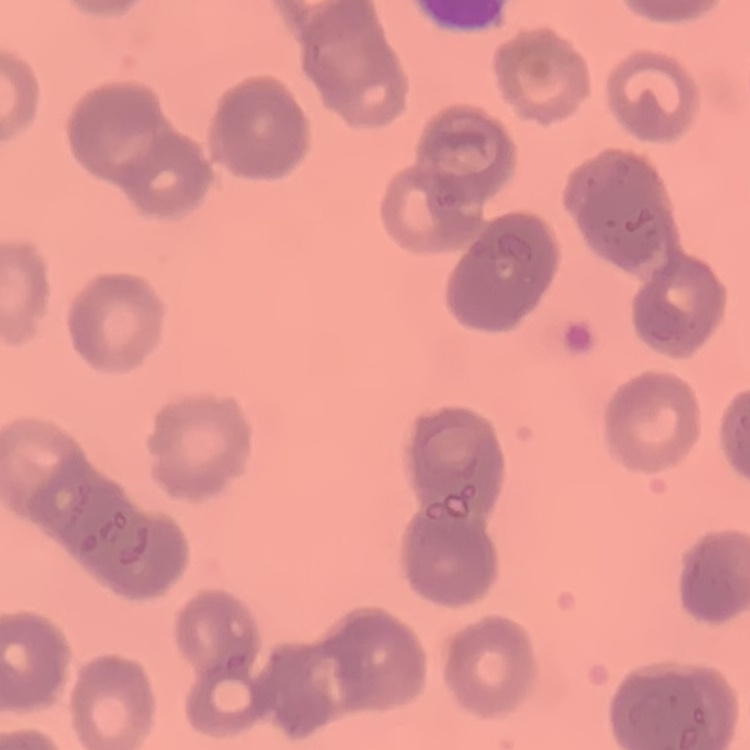

Summary:
  - Red blood cell morphology: rouleaux formation
  - Preparation: thin blood smear
  - Stain: Field's or Giemsa
  - Image type: one tile cut from a larger photomicrograph